Report the malaria status of this cell.
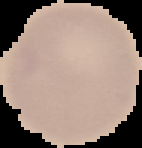

It is uninfected.

image type = segmented cell region with the area outside set to black
image size = 142×148 pixels
preparation = thin blood smear